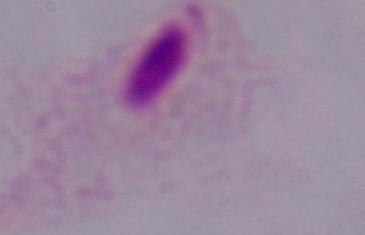
1000x magnification. A trichomonad is shown. Micrograph.